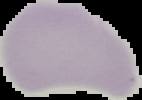

From a thin blood smear. Result: no Plasmodium parasites seen. Image is 142×100 pixels. Segmented cell region on a black background.